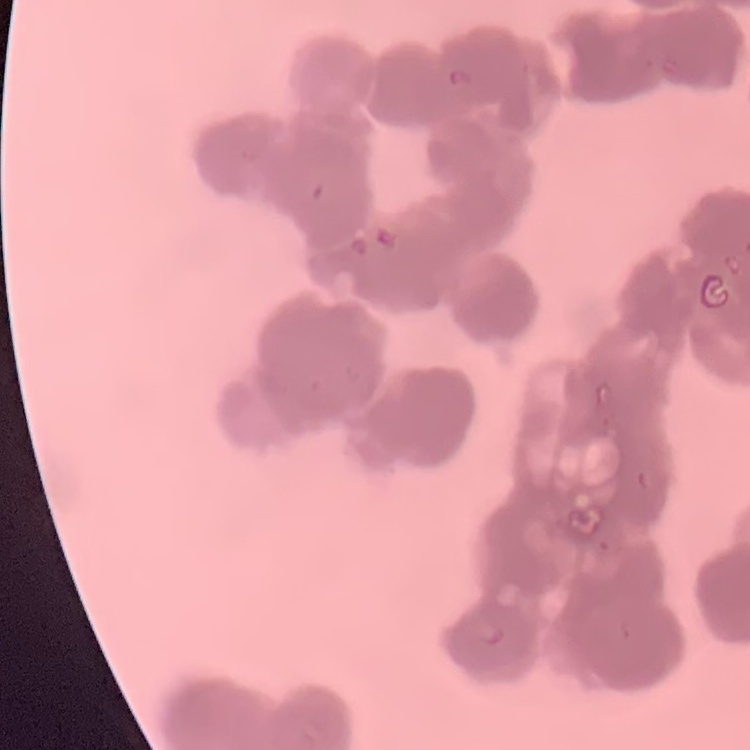

The red blood cells show rouleaux formation. Field's or Giemsa stain. Thin blood film. One tile cut from a larger photomicrograph.